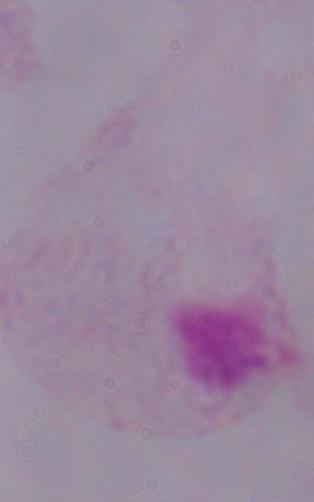

A trichomonad is seen. 1000x magnification. Micrograph.